Describe the morphology of the erythrocytes.
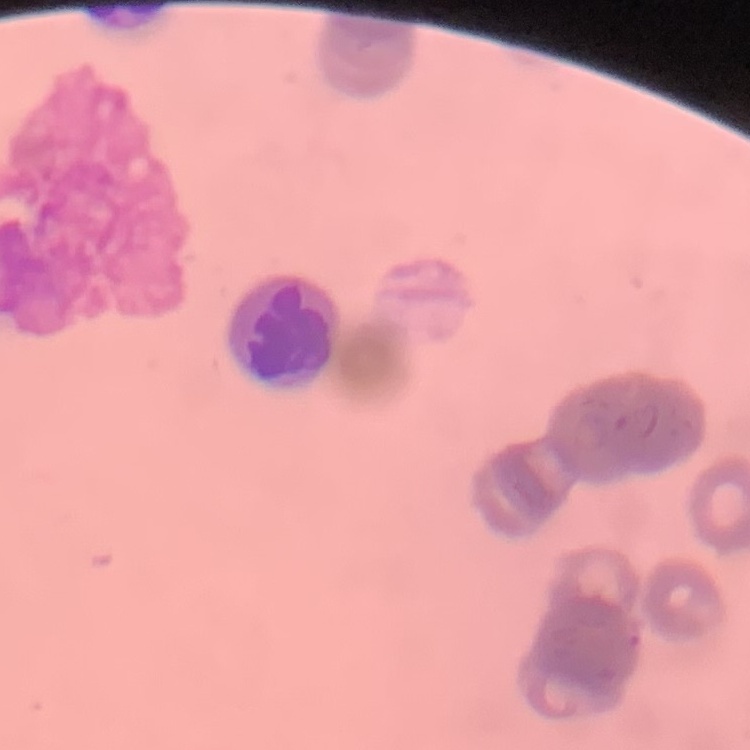

Rouleaux formation.

{
  "preparation": "thin blood film",
  "stain": "Field's or Giemsa",
  "image_type": "one tile cut from a larger photomicrograph"
}